Assess the morphology of the red blood cells.
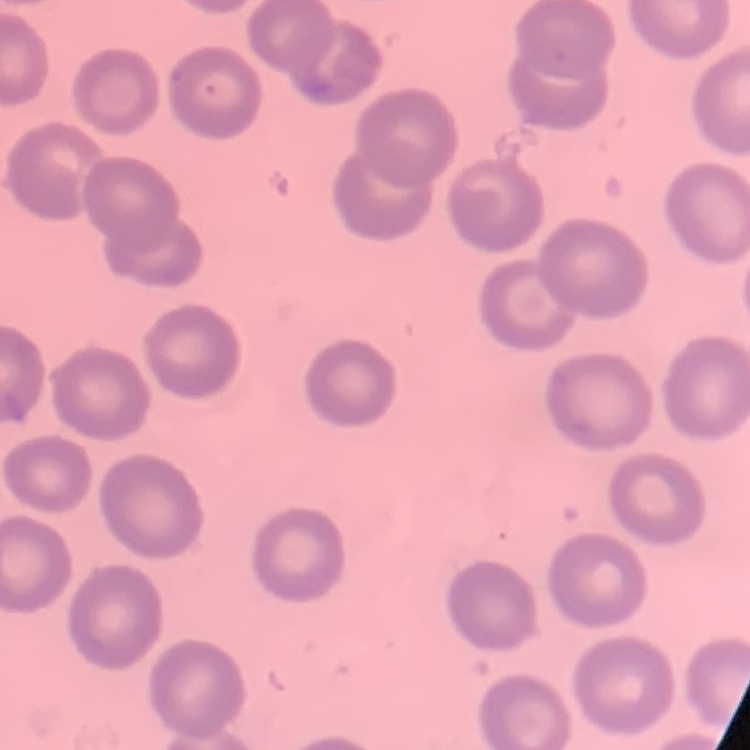
No rouleaux formation.

{
  "image_type": "square crop of a larger photomicrograph",
  "preparation": "thin peripheral smear",
  "stain": "Field's or Giemsa"
}